Locate every Plasmodium parasite.
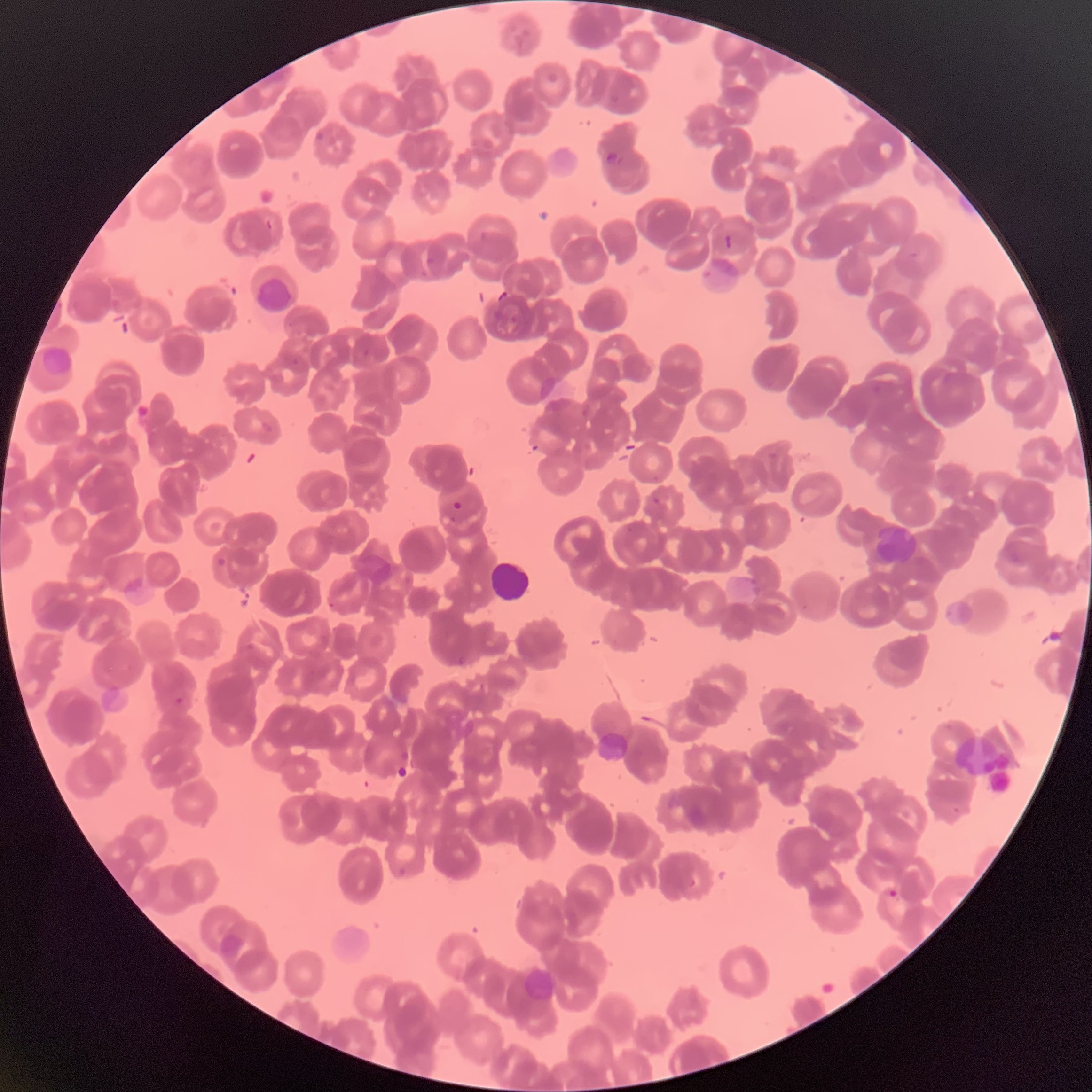
Approximate bounding boxes as [x1, y1, x2, y2] in pixels.
Plasmodium parasites: [603, 150, 625, 168], [529, 442, 545, 453], [652, 496, 661, 505], [452, 499, 463, 511], [217, 557, 228, 568], [327, 601, 337, 610], [453, 652, 471, 666], [174, 696, 185, 705], [887, 887, 900, 900].

white blood cell locations = [491, 562, 530, 603]
preparation = thin blood smear
image size = 1092×1092 pixels
modality = light microscopy
red blood cell morphology = rouleaux formation